State which cell type is depicted.
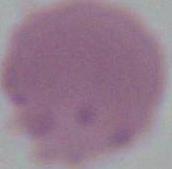

An erythrocyte.

{
  "magnification": "1000x",
  "modality": "micrograph"
}